Assess this cell for malaria.
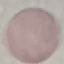
It is uninfected.

preparation = thin smear
stain = Giemsa
capture = smartphone through the microscope eyepiece
image type = cell patch, automatically extracted from a larger field of view and resized to 64 × 64 pixels